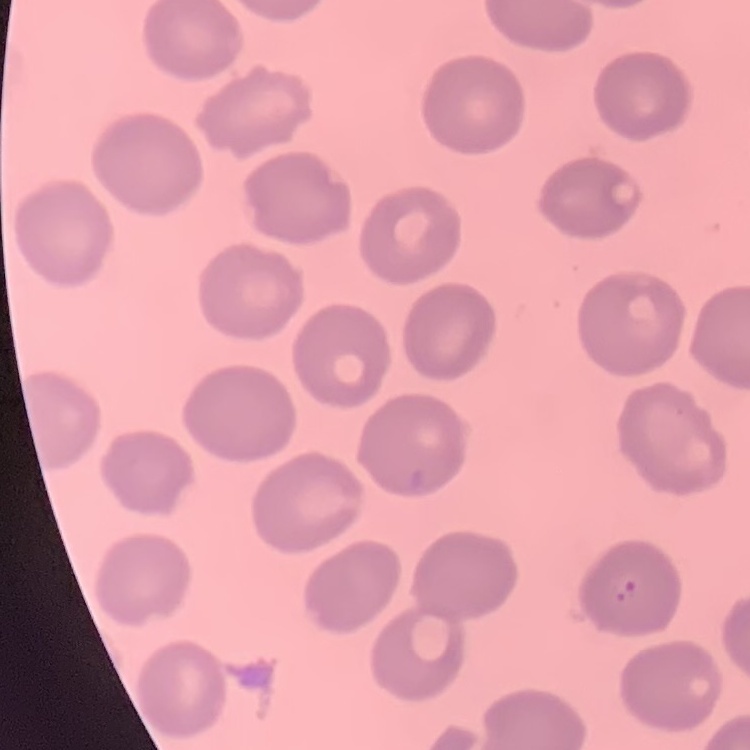

Summary:
  - Red blood cell morphology: no rouleaux formation
  - Stain: Field's or Giemsa
  - Image type: one tile cut from a larger photomicrograph
  - Preparation: thin peripheral smear